State which cell type is depicted.
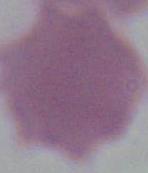
This is an erythrocyte.

1000x magnification. Micrograph.